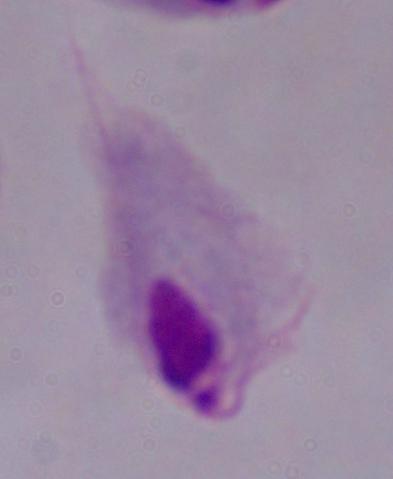

identification = trichomonad
magnification = 1000x
modality = photomicrograph